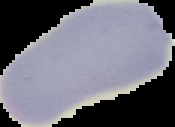
Summary:
  - Image size: 175×127 pixels
  - Image type: segmented cell region on a black background
  - Preparation: thin blood smear
  - Malaria status: uninfected